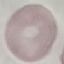

Summary:
  - Result: negative for malaria parasites
  - Preparation: thin smear
  - Capture: smartphone through the microscope eyepiece
  - Stain: Giemsa
  - Image type: cell patch, automatically extracted from a larger field of view and resized to 64 × 64 pixels